Outline each blood parasite and name the species.
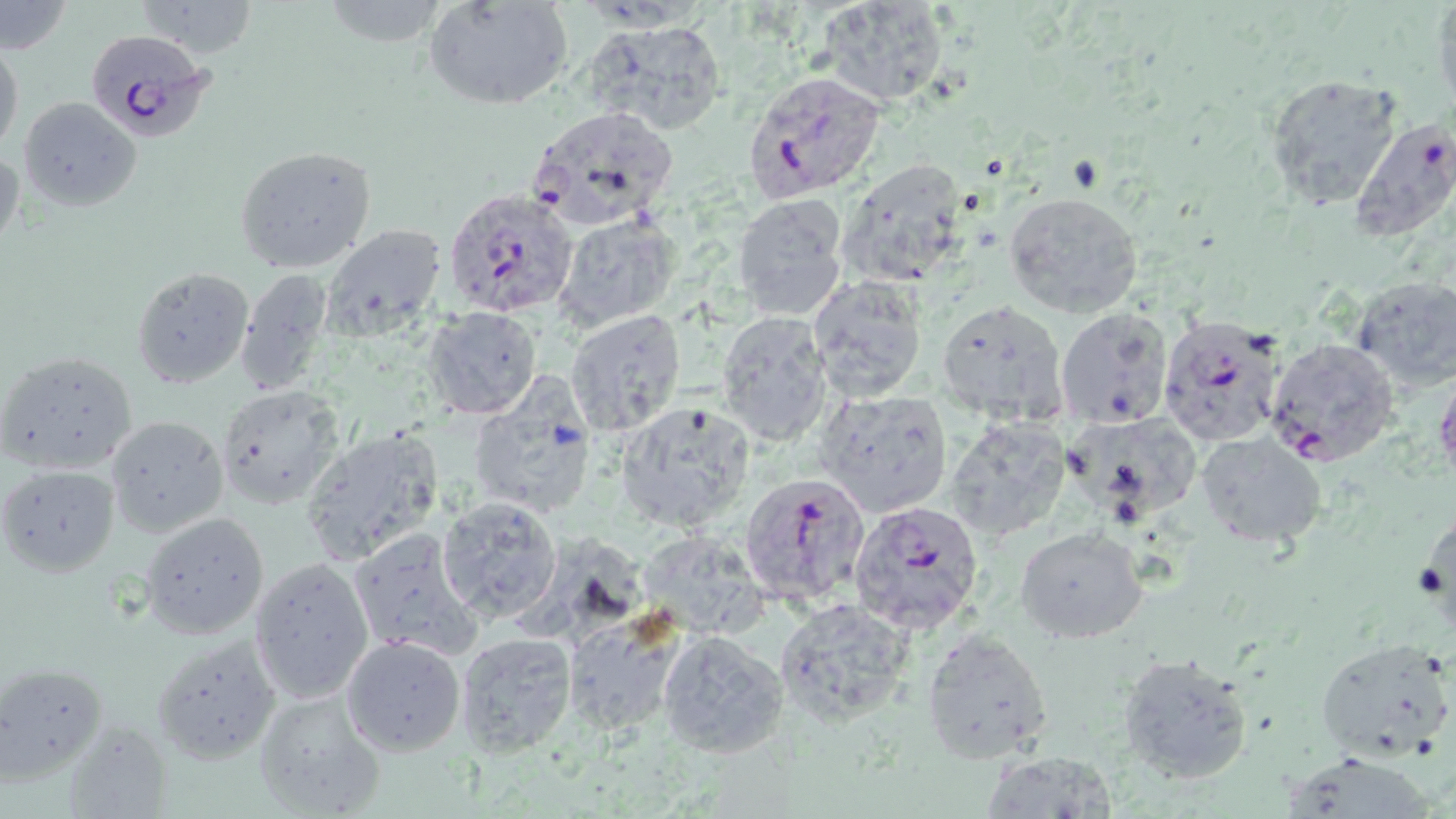

Approximate bounding boxes as [x1, y1, x2, y2] in pixels.
Plasmodium falciparum-infected red blood cells: [85, 29, 214, 143], [742, 70, 885, 202], [1347, 116, 1456, 242], [443, 186, 580, 320], [1159, 315, 1287, 446], [1264, 338, 1400, 467], [738, 472, 870, 610], [848, 501, 984, 635].
No Plasmodium ovale, Plasmodium malariae, Plasmodium vivax, Babesia divergens, or Trypanosoma brucei observed.

slide_level_diagnosis: Plasmodium falciparum
modality: light microscopy
magnification: 1000x
image_size: 1456×819 pixels
preparation: thin blood smear
stain: May-Grünwald-Giemsa
field_of_view: one of a larger specimen
uninfected_red_blood_cell_locations: 'approximate bounding boxes as [x1, y1, x2, y2] in pixels: [135, 0, 258, 61], [424, 0, 574, 110], [819, 0, 954, 108], [1433, 0, 1456, 114], [2, 2, 72, 53], [583, 21, 729, 138], [0, 39, 23, 159], [1265, 73, 1401, 207], [17, 96, 142, 212], [530, 105, 681, 232], [0, 143, 22, 261], [233, 145, 378, 274], [837, 157, 976, 287], [1005, 191, 1145, 320], [732, 193, 851, 320], [555, 213, 679, 331], [322, 222, 446, 336], [132, 266, 253, 388], [235, 268, 337, 393], [807, 274, 929, 401], [1350, 277, 1456, 392], [935, 299, 1071, 425], [425, 306, 542, 417], [1055, 306, 1176, 429], [565, 309, 687, 435], [716, 311, 835, 447], [0, 350, 138, 475], [466, 379, 597, 521], [216, 384, 345, 508], [815, 388, 955, 518], [614, 399, 757, 534], [1067, 409, 1204, 521], [106, 414, 229, 539], [943, 417, 1072, 544], [300, 426, 444, 565], [1195, 431, 1327, 548], [1, 464, 120, 575], [437, 495, 563, 623], [138, 511, 269, 639], [1015, 525, 1149, 644], [347, 526, 484, 661], [632, 528, 772, 640], [249, 558, 372, 703], [774, 597, 916, 725], [562, 609, 690, 733], [656, 628, 788, 757], [922, 628, 1054, 764], [453, 631, 578, 756], [150, 635, 280, 764], [341, 636, 465, 756], [1315, 637, 1455, 760], [1117, 652, 1253, 787], [0, 659, 112, 790], [252, 687, 386, 818], [978, 750, 1119, 819]'